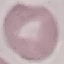

Result: no malaria parasites detected. Cell patch, automatically extracted from a larger field of view and resized to 64 × 64 pixels. Giemsa-stained preparation. Photographed with a smartphone camera at the microscope eyepiece. Thin blood film.